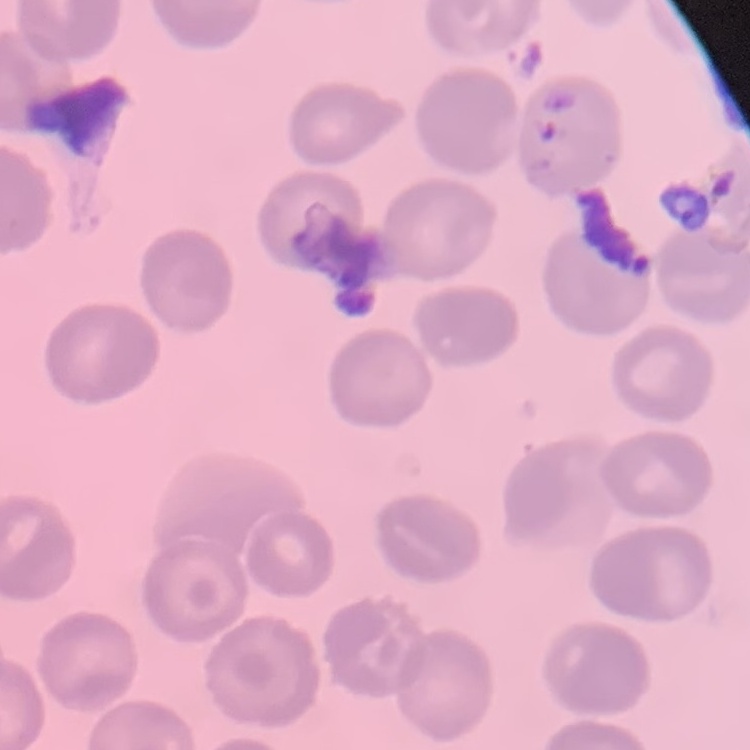
Summary:
  - Red blood cell morphology: no rouleaux formation
  - Stain: Field's or Giemsa
  - Preparation: thin peripheral smear
  - Image type: square crop of a larger photomicrograph